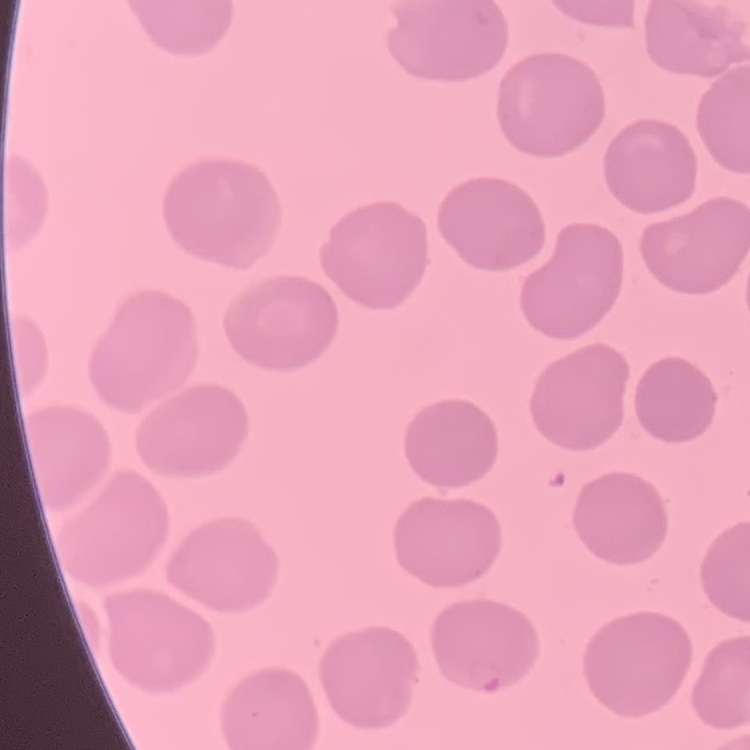
red blood cell morphology = no rouleaux formation
preparation = thin blood smear
stain = Field's or Giemsa
image type = square crop of a larger photomicrograph